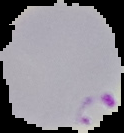 From a thin blood smear. Cell region segmented out of the field of view; the surrounding area is masked to black. Malaria status: parasitized. Image is 124×133 pixels.